Locate every malaria parasite.
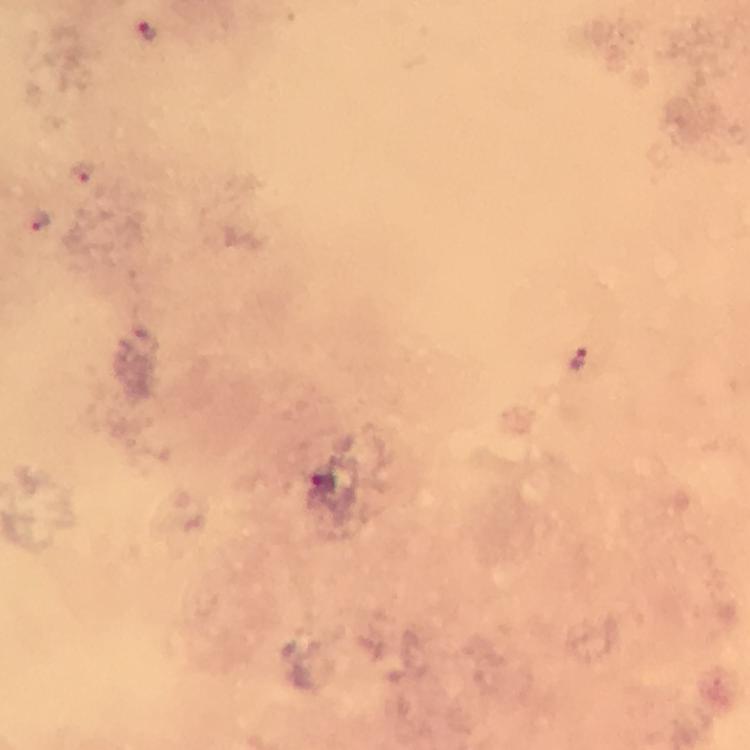
Approximate centers as (x, y) in pixels.
Malaria parasites: (148, 31), (84, 171), (40, 221), (579, 358).

Summary:
  - Capture: smartphone camera through the microscope
  - Stain: Giemsa
  - Immersion oil: applied
  - Magnification: 100x
  - Image size: 750×750 pixels
  - Preparation: thick smear
  - Context: from a malaria diagnostic workup
  - Cropped from: a single field of view